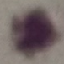
Result: negative for malaria parasites. Thin blood smear. Giemsa-stained preparation. Acquired by smartphone through the microscope eyepiece. Automatically extracted cell patch, resized to 64 × 64 pixels.